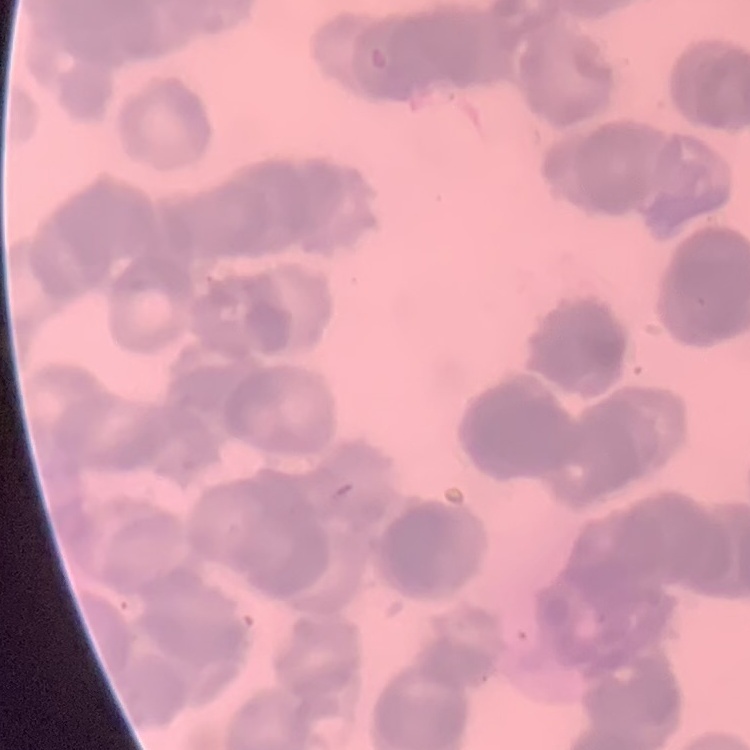
{
  "erythrocyte_morphology": "rouleaux formation",
  "stain": "Field's or Giemsa",
  "preparation": "thin blood film",
  "image_type": "one tile cut from a larger photomicrograph"
}